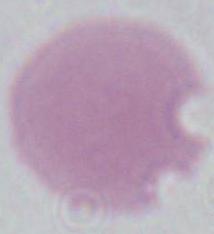 Captured at 1000x magnification. An erythrocyte is shown. Micrograph.